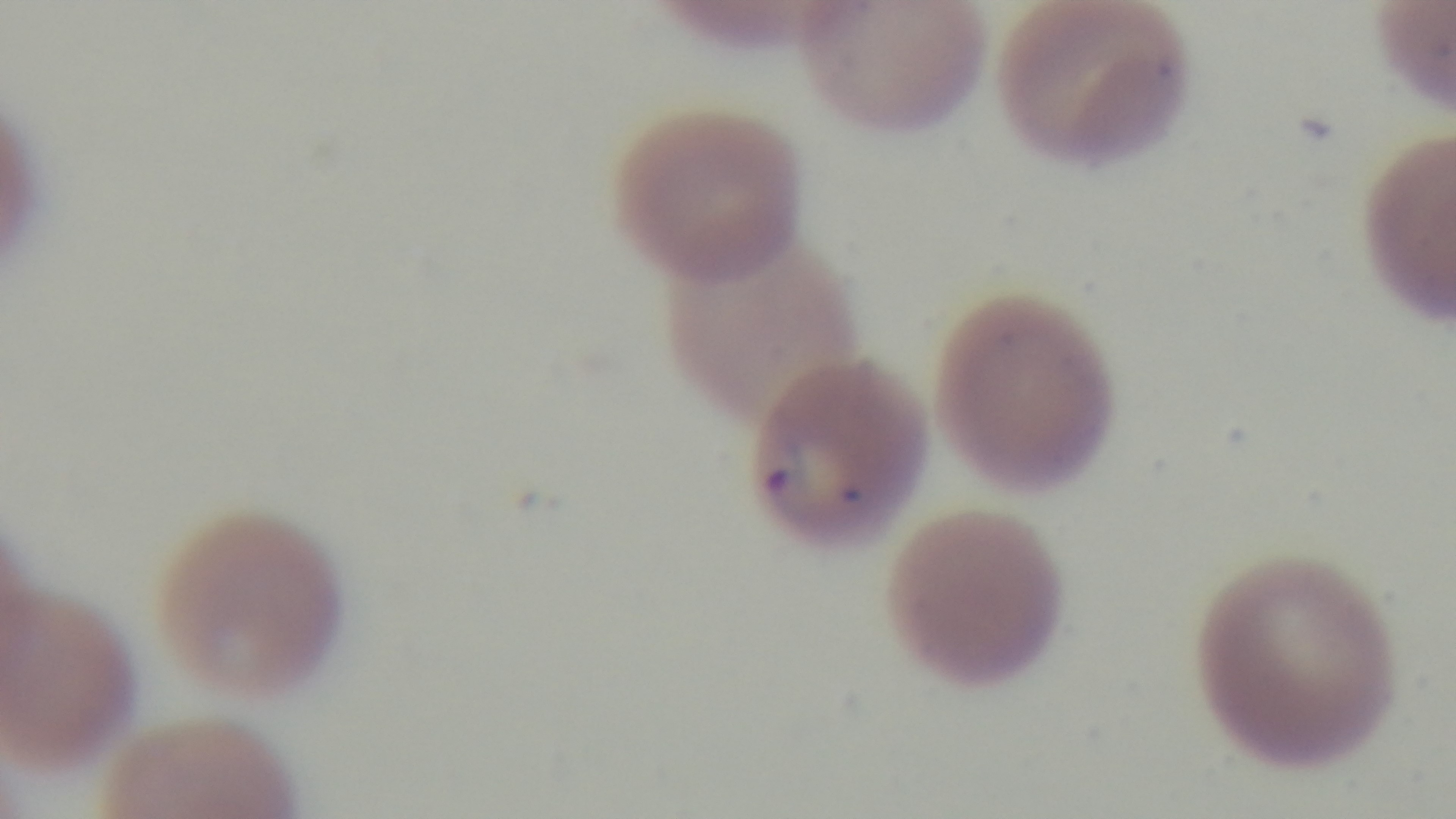
Preparation: thin smear. Giemsa-stained. Photomicrograph. Mounted 4K digital camera. 100x oil-immersion objective. Malaria status: positive. Single field of view.